Assess this cell for malaria.
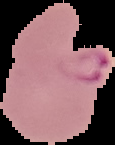
Parasitized.

Summary:
  - Image size: 115×145 pixels
  - Preparation: thin blood smear
  - Image type: segmented cell region with the area outside set to black